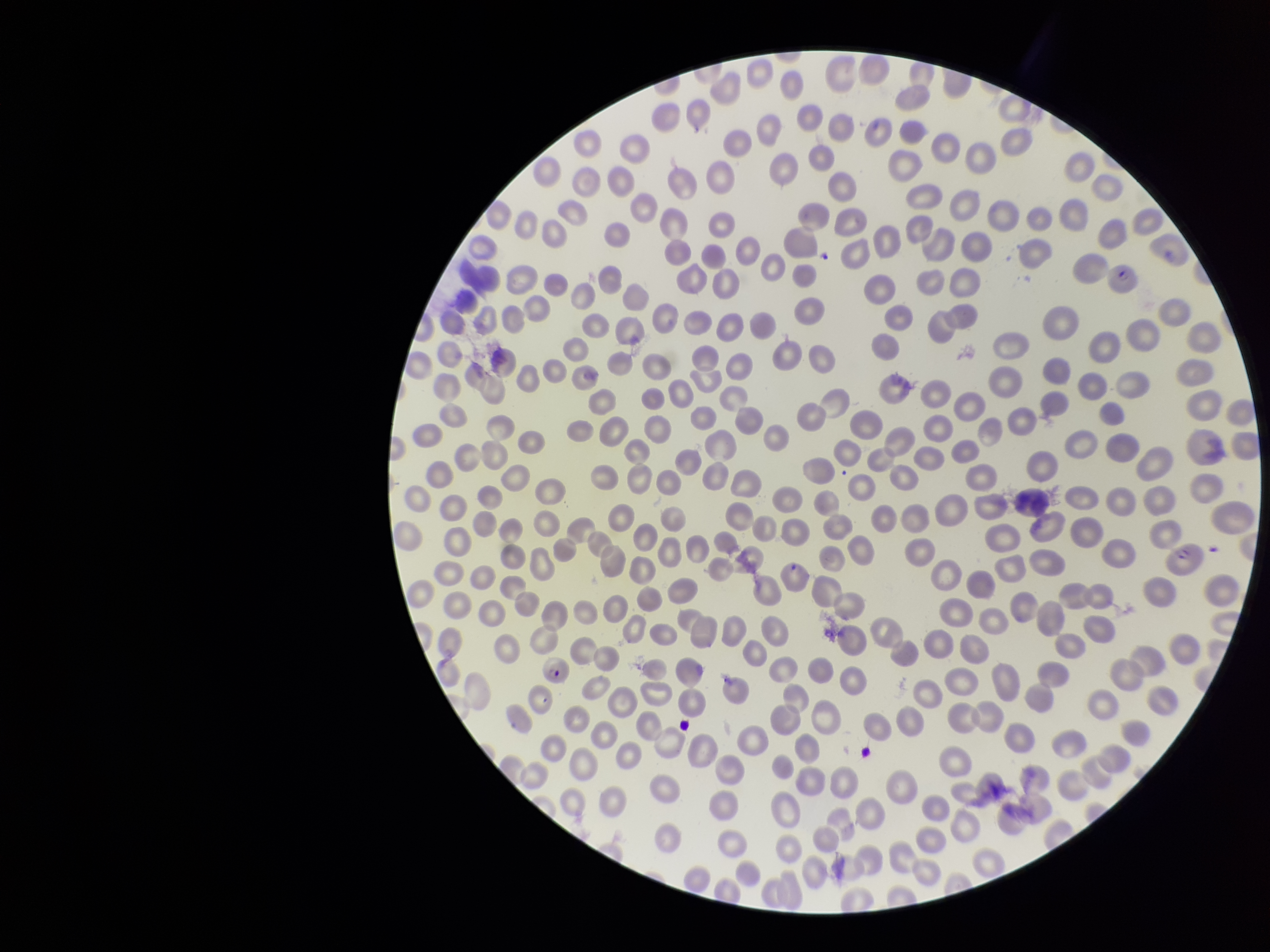

image size = 1270×952 pixels
red blood cell count = 318
stain = Giemsa
species reported for this patient = Plasmodium falciparum
preparation = thin blood smear
patient malaria status = infected
parasitized red blood cell count = 3
field of view = single
capture = smartphone photograph through the microscope eyepiece
parasitized red blood cells = detected